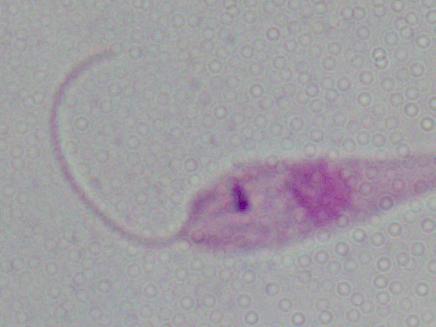 A Leishmania parasite is seen. Micrograph. 1000x magnification.